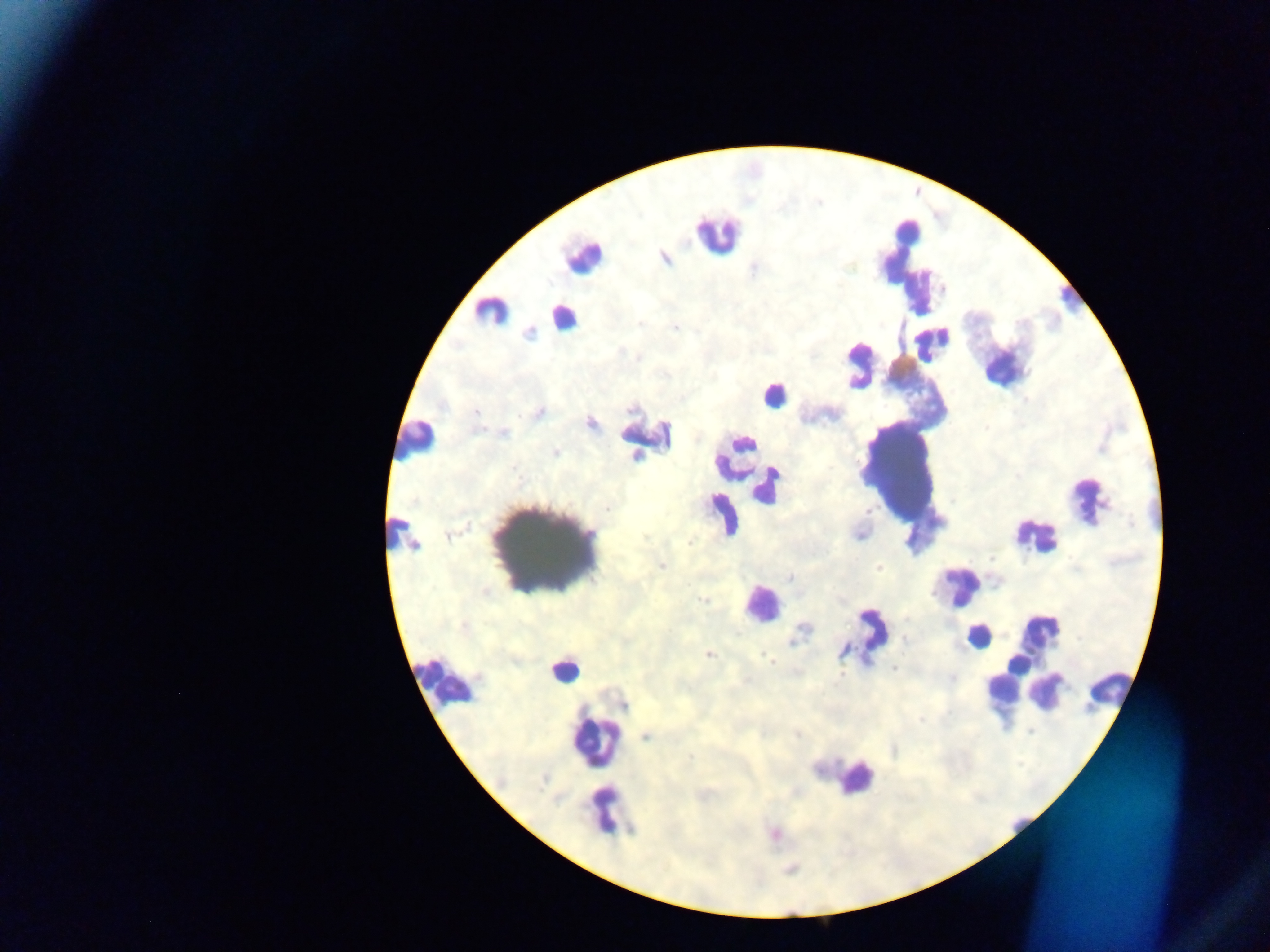

{
  "preparation": "thick blood film",
  "leukocyte_locations": "approximate centers as (x, y) in pixels: (717, 232), (579, 256), (491, 312), (567, 321), (777, 394), (416, 442), (905, 469), (1091, 498), (1035, 540), (548, 550), (960, 582), (763, 602), (1041, 627), (977, 637), (565, 671), (445, 685), (1114, 690), (1046, 691), (595, 742), (855, 782), (605, 811)",
  "capture": "mobile-phone photograph through a microscope",
  "country": "Ghana",
  "field_of_view": "single",
  "image_size": "1270×952 pixels",
  "malaria_parasite_locations": "approximate centers as (x, y) in pixels: (665, 259), (640, 322), (675, 327), (528, 335), (638, 356), (539, 413), (477, 414), (590, 422), (503, 433), (873, 435), (664, 436), (556, 452), (635, 454), (514, 469), (606, 510), (396, 524), (867, 536), (646, 538), (690, 541), (414, 545), (662, 565), (878, 566), (790, 577), (489, 591), (704, 600), (800, 635), (905, 639), (845, 649), (709, 655), (771, 658), (893, 667), (841, 671), (1029, 731), (797, 735), (645, 737), (689, 758), (706, 792), (702, 797)"
}